Locate every Plasmodium parasite.
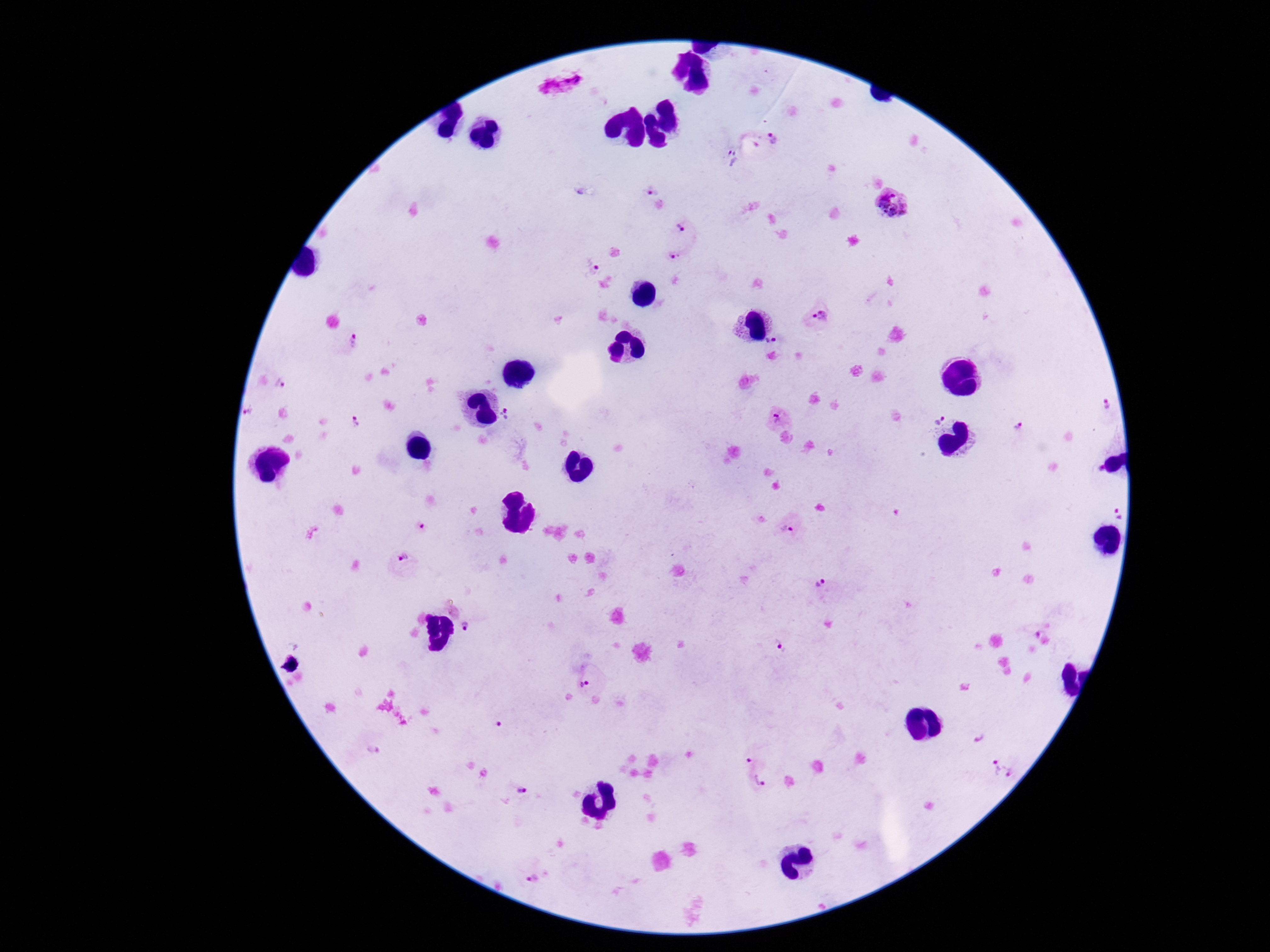

Approximate centers as [x, y] in pixels.
Plasmodium parasites: [774, 140], [729, 158], [646, 188], [892, 202], [683, 222], [680, 255], [588, 265], [818, 318], [773, 342], [351, 343], [277, 381], [1107, 400], [510, 411], [245, 414], [935, 416], [778, 418], [356, 423], [1017, 426], [1106, 508], [417, 527], [787, 528], [403, 563], [818, 584], [464, 627], [1033, 630], [778, 650], [588, 686], [494, 723], [980, 738], [370, 749], [749, 761], [992, 765], [1015, 771], [760, 785], [521, 795], [534, 872].

Summary:
  - Stain: Giemsa
  - Patient malaria status: positive
  - Preparation: thick peripheral-blood smear
  - Magnification: 100x
  - Capture: smartphone camera through the microscope eyepiece
  - Image size: 1270×952 pixels
  - Field of view: one from this slide